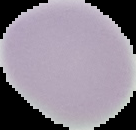

Summary:
  - Image type: segmented cell region on a black background
  - Preparation: thin blood smear
  - Image size: 136×130 pixels
  - Malaria status: uninfected